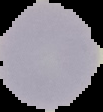
Summary:
  - Preparation: thin blood smear
  - Image size: 103×112 pixels
  - Malaria status: uninfected
  - Image type: segmented cell region with the area outside set to black